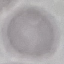 Result: negative for malaria parasites. Acquired by smartphone through the microscope eyepiece. Thin blood smear. Giemsa stain. Automatically extracted cell patch, resized to 64 × 64 pixels.